Assess the morphology of the erythrocytes.
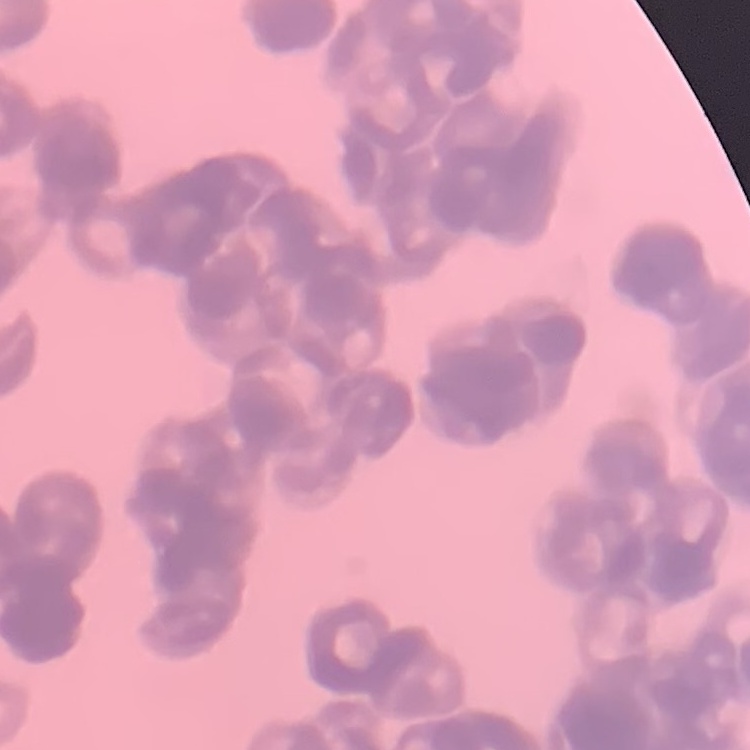

They show rouleaux formation.

{
  "preparation": "thin blood film",
  "image_type": "one tile cut from a larger photomicrograph",
  "stain": "Field's or Giemsa"
}